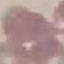
malaria status = uninfected
image type = automatically extracted cell patch, resized to 64 × 64 pixels
preparation = thin blood smear
capture = smartphone camera at the microscope eyepiece
stain = Giemsa